Point out each malaria parasite.
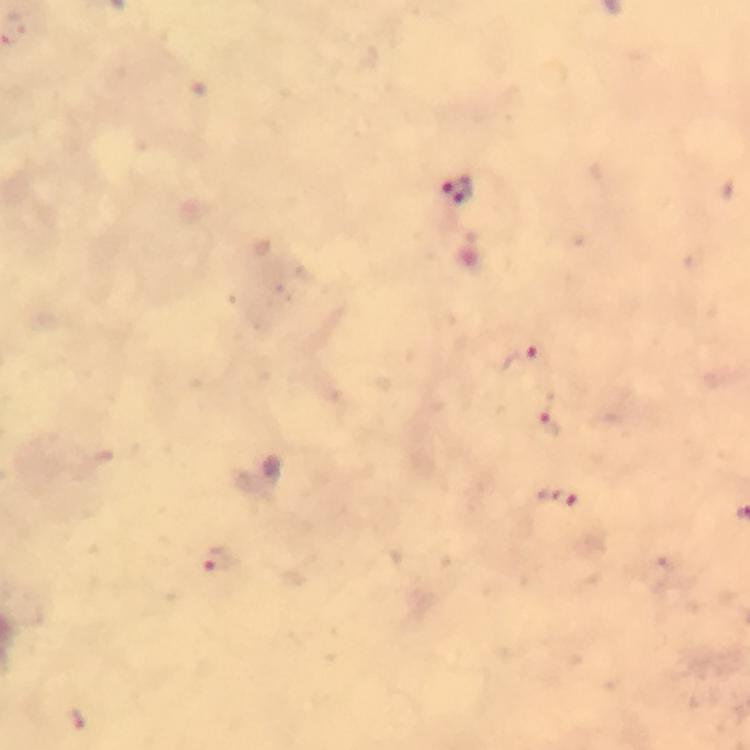

Approximate object centers, in pixels from the top-left corner.
Malaria parasites: (x=455, y=190), (x=522, y=357), (x=553, y=421), (x=559, y=498), (x=219, y=561), (x=78, y=719).

Summary:
  - Cropped from: a single field of view
  - Stain: Giemsa
  - Capture: smartphone photograph through a microscope
  - Image size: 750×750 pixels
  - Preparation: thick blood smear
  - Context: from a diagnostic examination for malaria
  - Magnification: 100x
  - Immersion oil: used